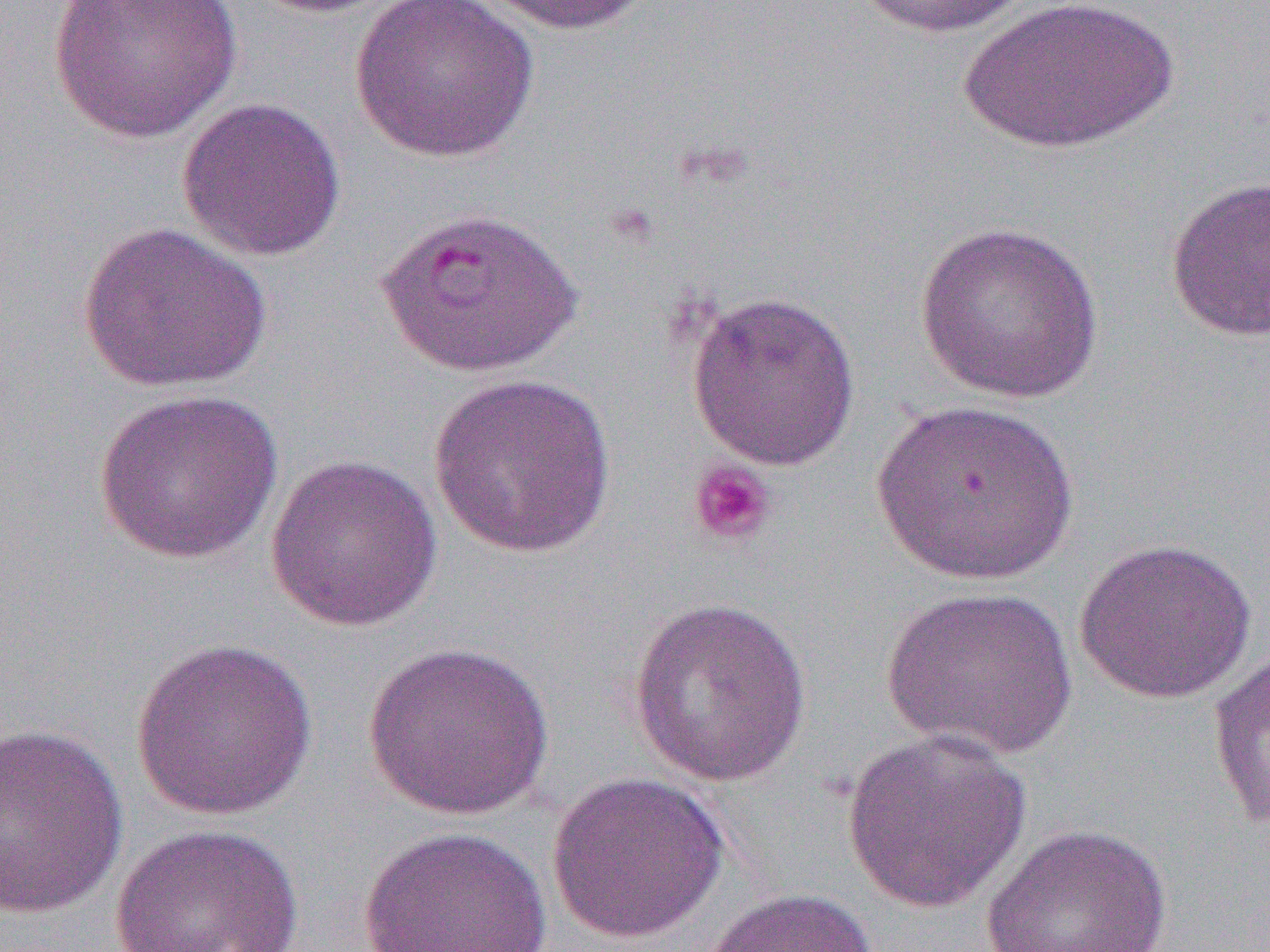
Approximate bounding boxes as [x1, y1, x2, y2] in pixels. Uninfected red blood cell locations: [48, 0, 245, 144], [247, 0, 406, 17], [348, 0, 541, 164], [477, 0, 655, 36], [847, 0, 1036, 40], [957, 0, 1182, 157], [176, 96, 347, 262], [1164, 175, 1270, 342], [376, 205, 583, 378], [913, 219, 1105, 404], [78, 221, 273, 394], [685, 290, 861, 470], [427, 372, 617, 559], [92, 388, 285, 565], [872, 399, 1078, 586], [265, 453, 443, 633], [1073, 537, 1258, 706], [881, 586, 1076, 760], [628, 597, 813, 788], [1207, 635, 1270, 835], [129, 637, 318, 821], [362, 642, 555, 820], [1, 723, 128, 920], [840, 727, 1034, 913], [546, 770, 729, 945], [109, 822, 306, 952], [981, 823, 1172, 952], [357, 825, 553, 952], [701, 887, 878, 952]. Platelet locations: [687, 458, 778, 547]. Slide-level diagnosis: Plasmodium falciparum. Thin blood smear. Light microscopy. Image is 1270×952 pixels. 1000x magnification. Single field of view.